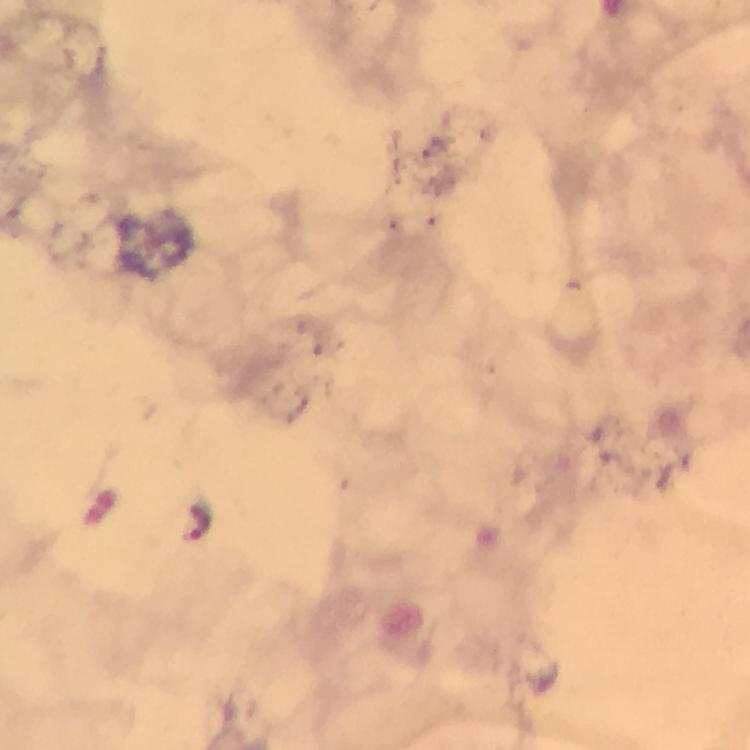

{
  "stain": "Giemsa",
  "magnification": "100x",
  "immersion_oil": "applied",
  "plasmodium_parasite_locations": "approximate centers as {x, y} in pixels: {196, 522}",
  "context": "from a diagnostic examination for malaria",
  "preparation": "thick blood film",
  "capture": "smartphone camera through the microscope",
  "image_size": "750×750 pixels",
  "cropped_from": "a single field of view"
}